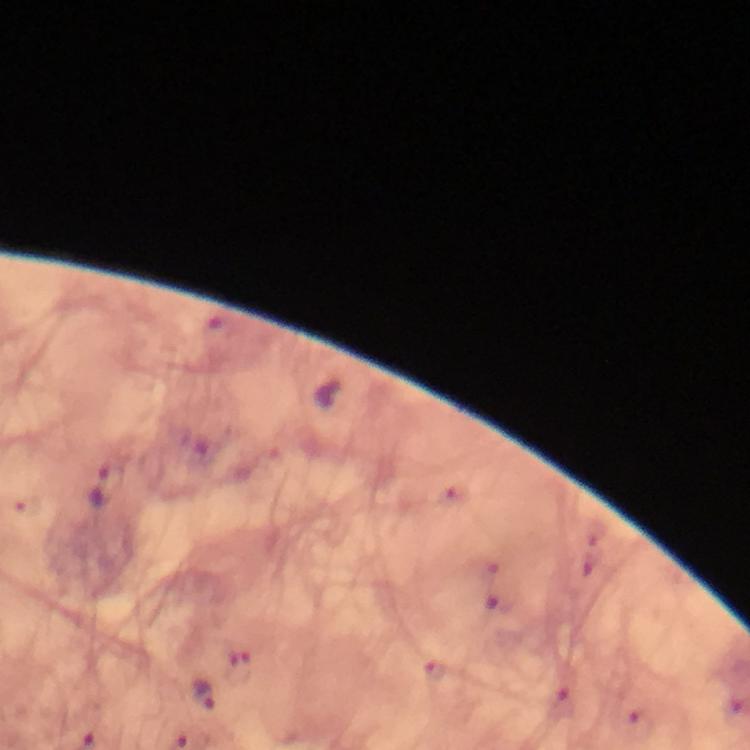
Approximate object centers, in pixels from the top-left corner. Plasmodium parasite locations: (x=106, y=483), (x=433, y=668), (x=205, y=698), (x=565, y=706). From a malaria diagnostic workup. Immersion oil was used. Giemsa-stained preparation. A crop from one field of view. Thick blood film. Smartphone photograph taken through a microscope. Image is 750×750 pixels. At 100x magnification.